Assess the morphology of the erythrocytes.
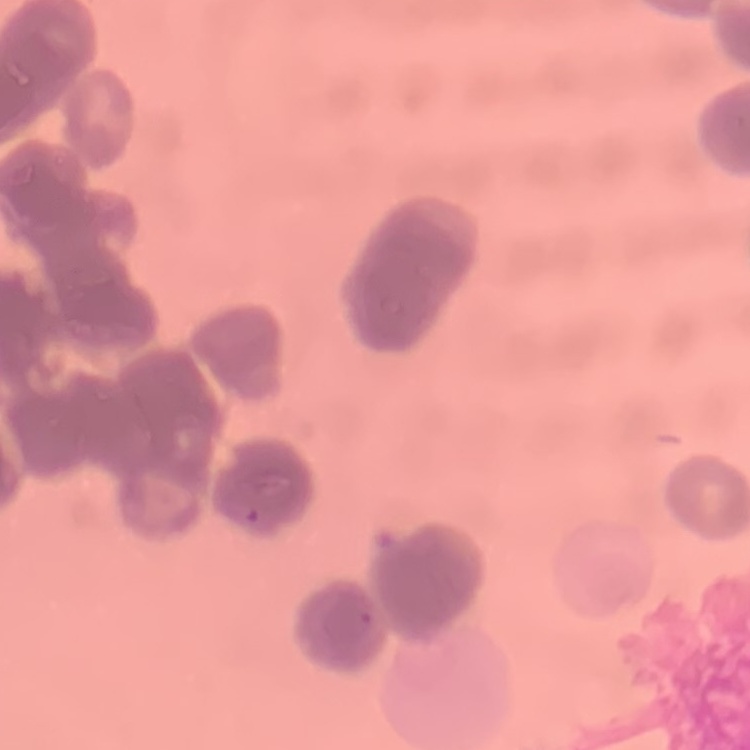
They show rouleaux formation.

Stained with either Field's or Giemsa. One tile cut from a larger photomicrograph. Thin blood smear.